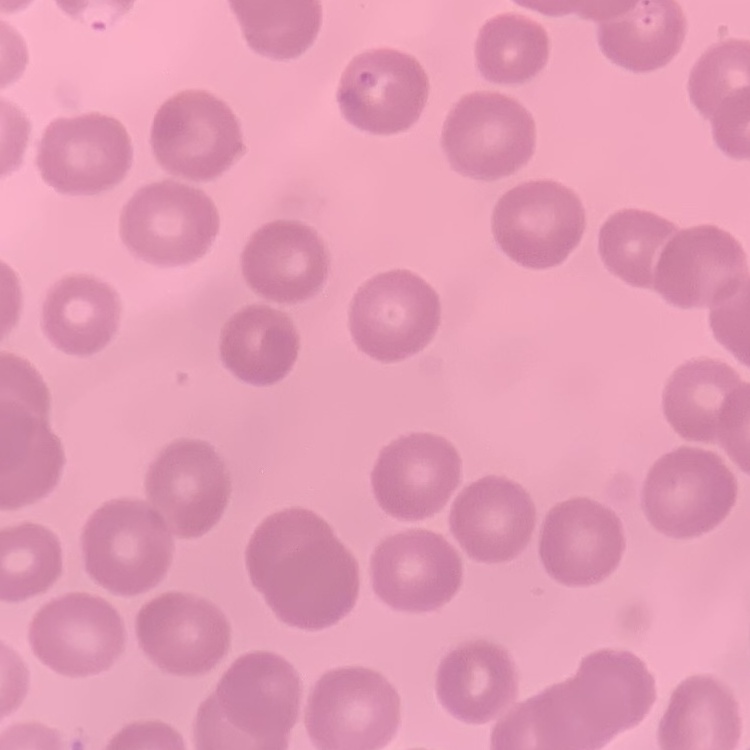
red blood cell morphology = no rouleaux formation
image type = square crop of a larger photomicrograph
preparation = thin blood film
stain = Field's or Giemsa